State which parasite is depicted.
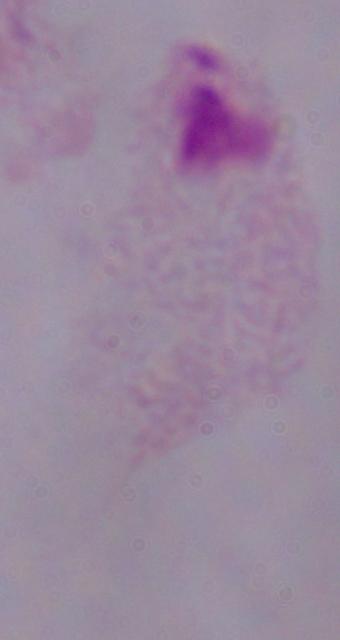
This is a trichomonad.

magnification = 1000x
modality = micrograph